Comment on the morphology of the erythrocytes.
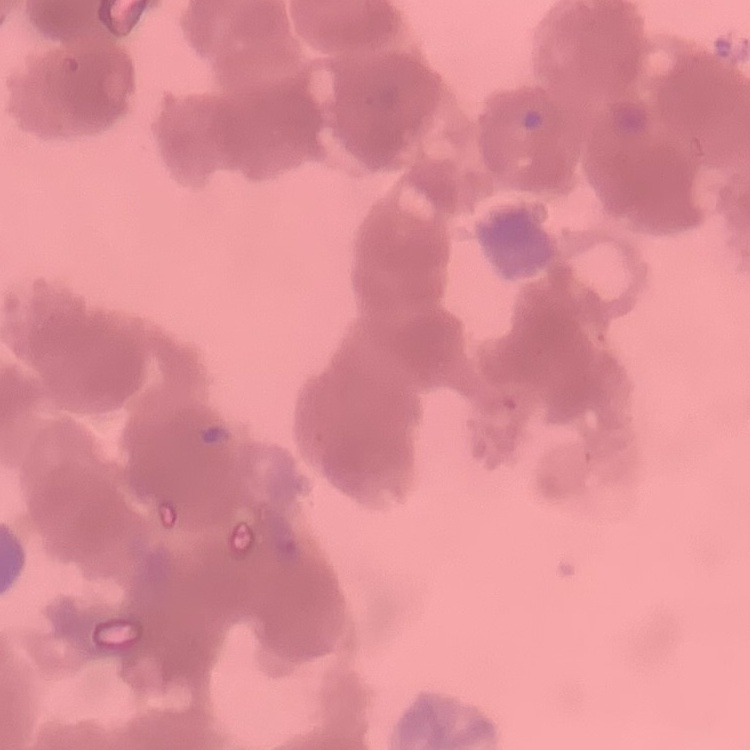

Rouleaux formation.

Stained with either Field's or Giemsa. Thin blood film. Square crop of a larger photomicrograph.